Outline each Plasmodium ovale-infected red blood cell.
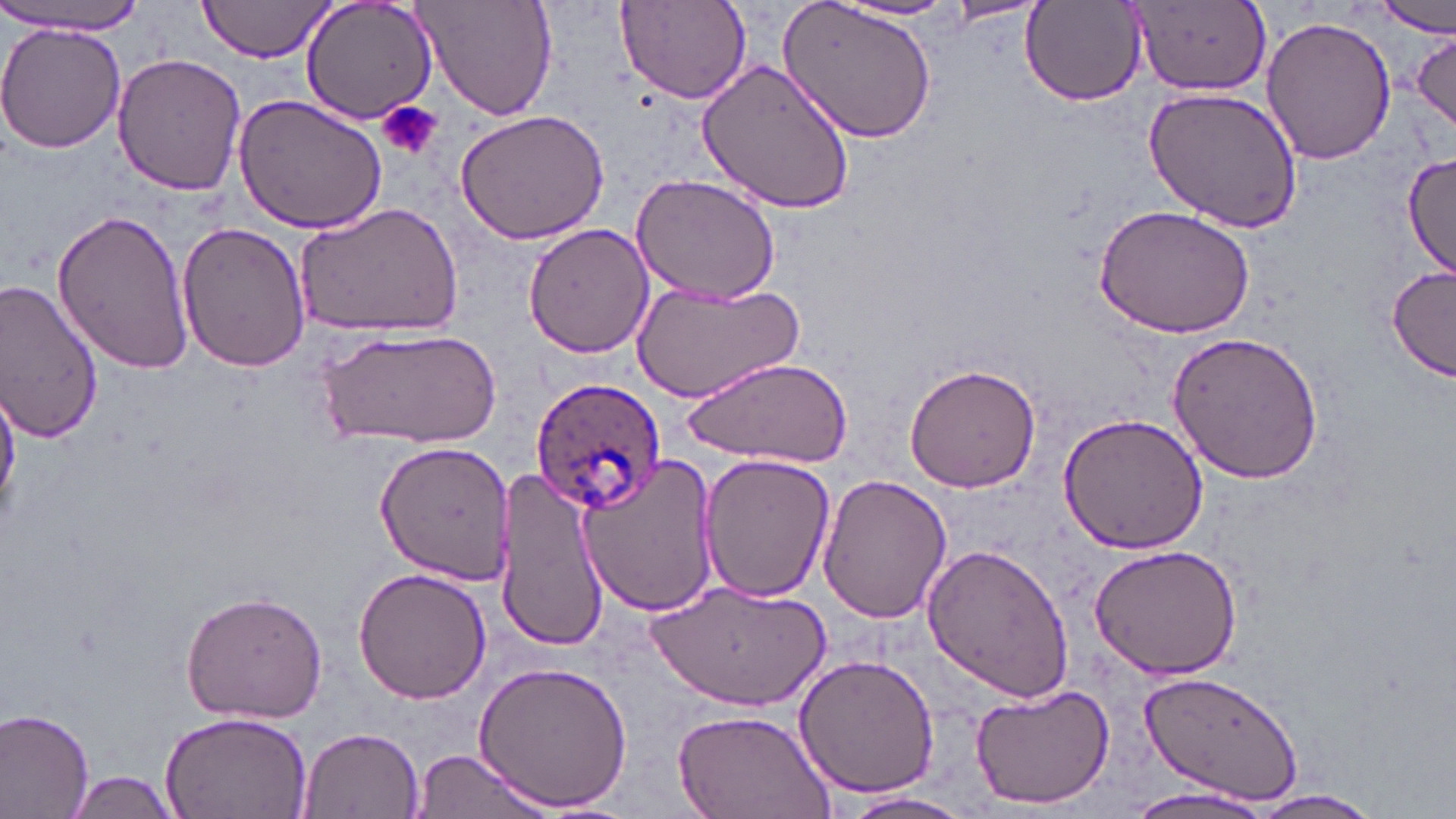

Approximate bounding boxes as named x1/y1/x2/y2 corners in pixels.
Plasmodium ovale-infected red blood cells: (x1=530, y1=377, x2=665, y2=514).

Platelet locations: (x1=377, y1=101, x2=443, y2=161). Uninfected red blood cell locations: (x1=197, y1=0, x2=337, y2=61), (x1=300, y1=0, x2=440, y2=126), (x1=413, y1=0, x2=558, y2=120), (x1=780, y1=0, x2=938, y2=142), (x1=615, y1=1, x2=752, y2=105), (x1=835, y1=1, x2=967, y2=23), (x1=941, y1=1, x2=1048, y2=26), (x1=1126, y1=1, x2=1273, y2=97), (x1=1373, y1=1, x2=1455, y2=38), (x1=1020, y1=3, x2=1147, y2=106), (x1=0, y1=6, x2=150, y2=35), (x1=1262, y1=14, x2=1397, y2=165), (x1=0, y1=24, x2=126, y2=155), (x1=1410, y1=30, x2=1456, y2=134), (x1=113, y1=53, x2=248, y2=195), (x1=697, y1=57, x2=858, y2=214), (x1=1143, y1=86, x2=1304, y2=234), (x1=232, y1=94, x2=388, y2=237), (x1=454, y1=109, x2=611, y2=245), (x1=1401, y1=150, x2=1456, y2=279), (x1=632, y1=174, x2=781, y2=305), (x1=294, y1=202, x2=463, y2=339), (x1=1092, y1=204, x2=1255, y2=339), (x1=51, y1=208, x2=192, y2=375), (x1=176, y1=221, x2=311, y2=374), (x1=522, y1=222, x2=657, y2=359), (x1=1387, y1=266, x2=1454, y2=383), (x1=631, y1=277, x2=805, y2=403), (x1=0, y1=281, x2=104, y2=442), (x1=323, y1=325, x2=496, y2=448), (x1=1165, y1=329, x2=1325, y2=484), (x1=689, y1=354, x2=854, y2=466), (x1=904, y1=363, x2=1041, y2=493), (x1=1, y1=380, x2=21, y2=522), (x1=1057, y1=410, x2=1210, y2=554), (x1=375, y1=438, x2=514, y2=582), (x1=699, y1=454, x2=835, y2=602), (x1=577, y1=456, x2=720, y2=619), (x1=496, y1=471, x2=610, y2=648), (x1=815, y1=472, x2=952, y2=625), (x1=922, y1=541, x2=1075, y2=704), (x1=1088, y1=543, x2=1243, y2=681), (x1=352, y1=568, x2=491, y2=704), (x1=646, y1=580, x2=831, y2=708), (x1=179, y1=589, x2=329, y2=724), (x1=793, y1=654, x2=941, y2=799), (x1=473, y1=659, x2=633, y2=810), (x1=1137, y1=669, x2=1306, y2=806), (x1=968, y1=681, x2=1116, y2=810), (x1=0, y1=706, x2=95, y2=819), (x1=161, y1=708, x2=313, y2=819), (x1=670, y1=710, x2=834, y2=819), (x1=298, y1=727, x2=425, y2=819), (x1=409, y1=748, x2=553, y2=819), (x1=63, y1=770, x2=183, y2=818), (x1=1130, y1=785, x2=1276, y2=819), (x1=839, y1=790, x2=978, y2=818), (x1=1238, y1=790, x2=1385, y2=818). Slide-level diagnosis: Plasmodium ovale. Single field of view. Captured at 1000x magnification. Image is 1456×819 pixels. May-Grünwald-Giemsa stain. Optical microscopy. Thin blood smear.